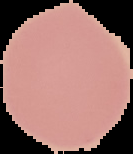 Image is 133×154 pixels. Result: no Plasmodium parasites seen. Segmented cell region on a black background. From a thin blood smear.